Locate every Plasmodium falciparum-infected red blood cell.
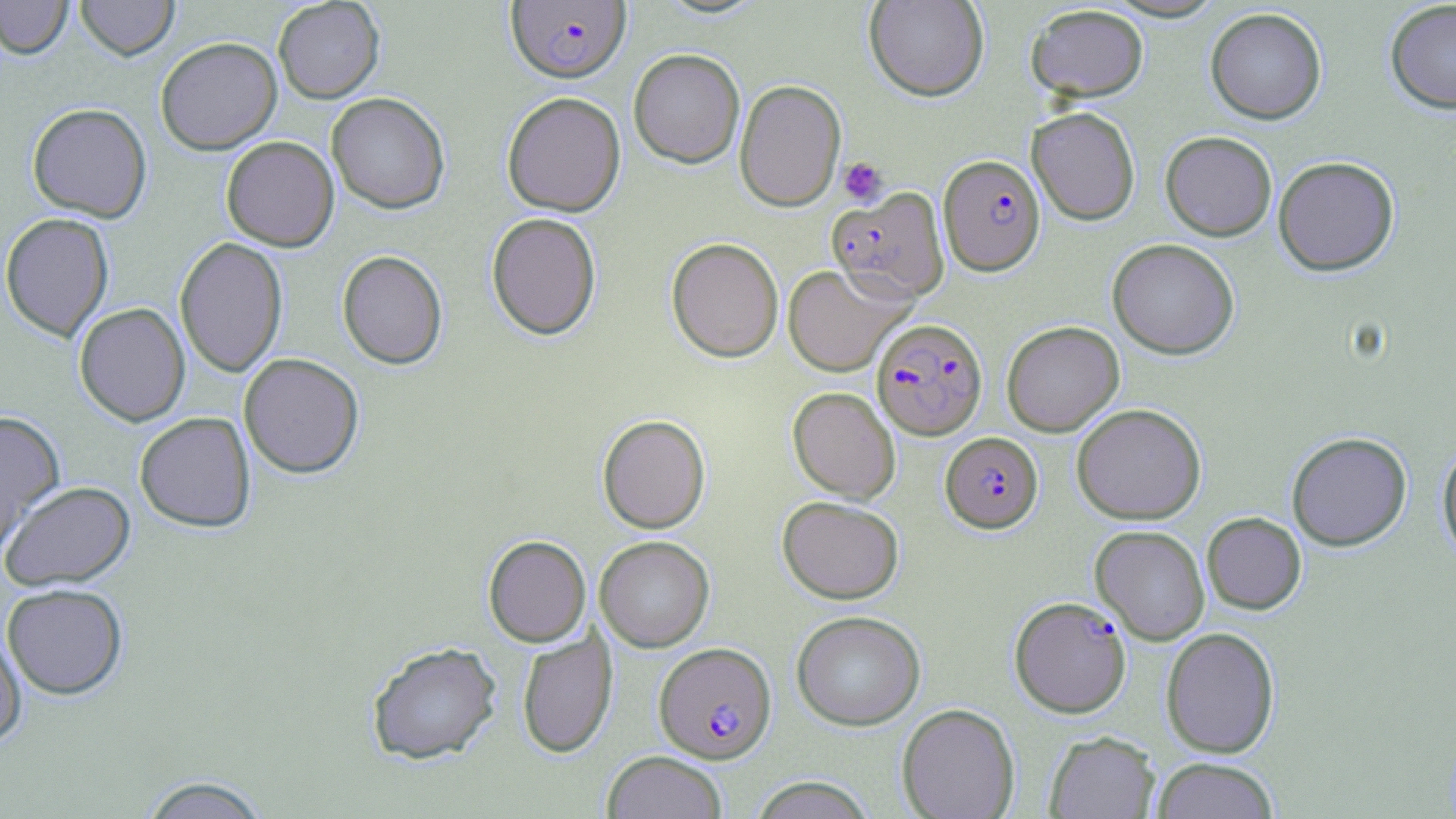
Approximate bounding boxes as (x1,y1)-(x2,y2) corner pairs in pixels.
Plasmodium falciparum-infected red blood cells: (506,1)-(631,83), (938,154)-(1045,276), (826,187)-(950,304), (872,319)-(988,439), (941,432)-(1042,532), (1010,596)-(1131,717), (654,641)-(776,763).

slide_level_diagnosis: Plasmodium falciparum
modality: optical microscopy
image_size: 1456×819 pixels
stain: May-Grünwald-Giemsa
platelet_locations: 'approximate bounding boxes as (x1,y1)-(x2,y2) corner pairs in pixels: (838,157)-(888,206)'
magnification: 1000x
uninfected_red_blood_cell_locations: 'approximate bounding boxes as (x1,y1)-(x2,y2) corner pairs in pixels: (0,0)-(74,60), (76,0)-(179,60), (273,0)-(385,103), (864,0)-(988,101), (1385,1)-(1456,113), (1026,4)-(1148,101), (1205,7)-(1327,124), (155,36)-(282,155), (628,48)-(745,168), (734,79)-(846,211), (501,91)-(626,216), (326,92)-(450,214), (27,102)-(152,222), (1027,107)-(1140,225), (1160,131)-(1277,240), (221,136)-(339,251), (1273,156)-(1399,276), (486,212)-(601,340), (0,213)-(114,341), (174,237)-(288,377), (666,237)-(784,362), (1107,238)-(1239,359), (337,250)-(448,370), (782,264)-(912,377), (74,303)-(190,426), (1002,320)-(1124,436), (239,353)-(364,478), (788,387)-(900,502), (1071,403)-(1206,524), (0,410)-(65,552), (134,412)-(256,532), (597,414)-(710,533), (1286,431)-(1412,551), (1437,442)-(1456,564), (1,480)-(135,590), (777,496)-(904,604), (1202,512)-(1306,614), (1091,525)-(1210,644), (483,535)-(591,647), (595,535)-(714,652), (2,583)-(128,699), (791,610)-(925,730), (0,624)-(27,747), (1161,627)-(1280,757), (516,628)-(617,759), (365,641)-(502,765), (896,703)-(1020,819), (1044,731)-(1160,818), (602,750)-(728,819), (1150,757)-(1280,818), (137,774)-(273,819), (750,776)-(875,818)'
preparation: thin blood smear
field_of_view: single